Report the malaria status of this cell.
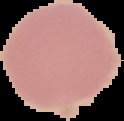

Uninfected.

Summary:
  - Preparation: thin blood film
  - Image size: 124×121 pixels
  - Image type: segmented cell region with the area outside set to black